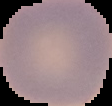
From a thin blood film. Malaria status: uninfected. Image is 112×106 pixels. Cell region segmented out of the field of view; the surrounding area is masked to black.